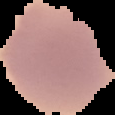
image type = segmented cell region on a black background
image size = 115×115 pixels
preparation = thin blood film
malaria status = uninfected